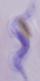
A trypanosome is seen. Micrograph. 1000x magnification.